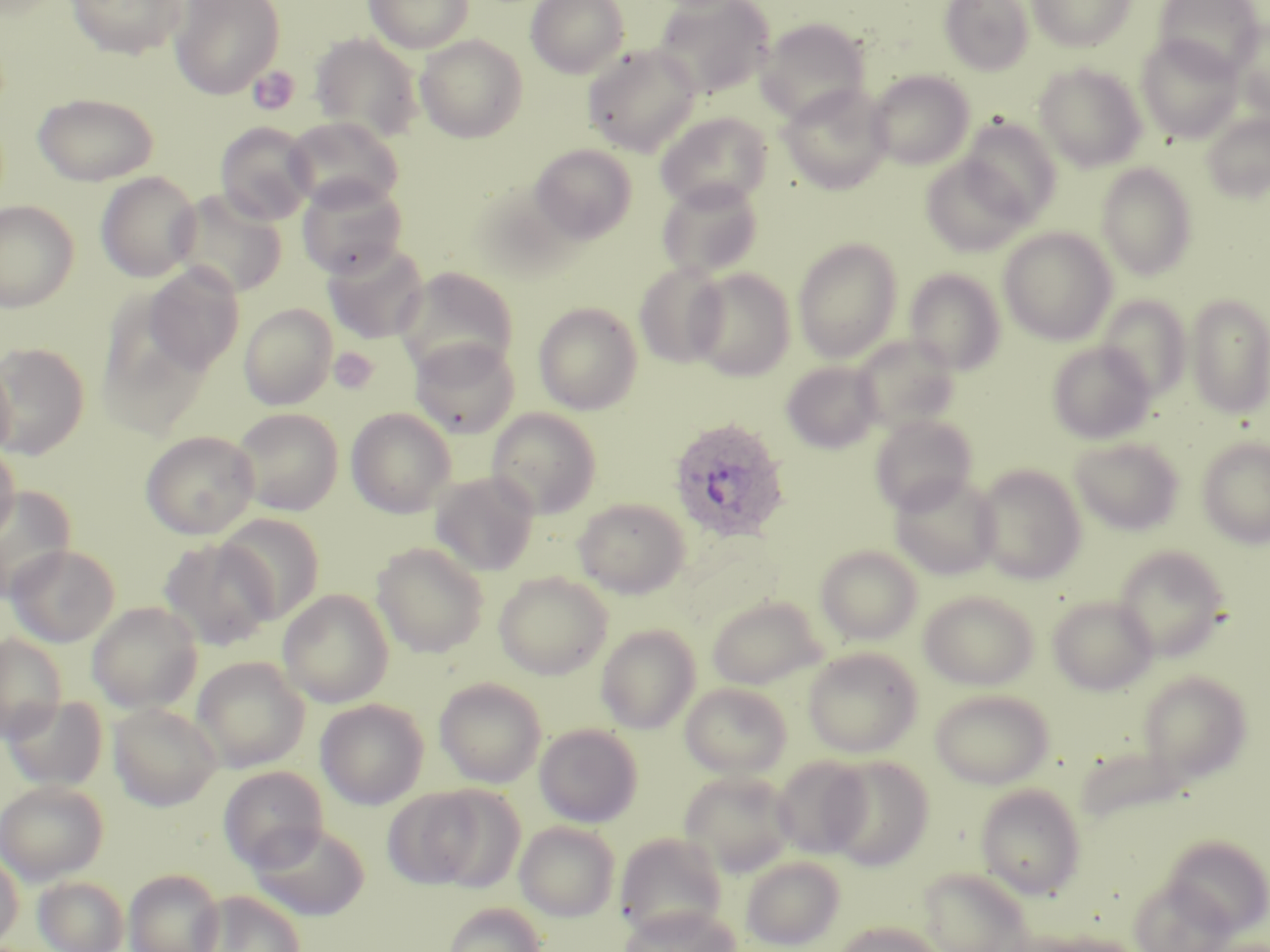

Approximate bounding boxes as (x1,y1)-(x2,y2) corner pairs in pixels. Platelet locations: (247,65)-(300,116), (329,347)-(380,394). Uninfected red blood cell locations: (67,0)-(188,59), (170,0)-(285,98), (363,0)-(474,52), (526,0)-(629,78), (654,0)-(775,99), (940,0)-(1034,75), (1027,0)-(1136,51), (1154,0)-(1263,77), (756,17)-(871,124), (1229,18)-(1270,119), (310,32)-(424,142), (415,35)-(528,142), (1136,35)-(1243,142), (582,43)-(702,156), (1034,63)-(1146,171), (867,70)-(975,170), (778,84)-(892,194), (32,92)-(159,186), (656,112)-(772,211), (1201,112)-(1270,203), (285,116)-(404,212), (959,117)-(1062,225), (215,122)-(317,225), (530,143)-(637,244), (920,155)-(1031,256), (1095,162)-(1199,280), (95,171)-(202,282), (297,176)-(408,279), (656,179)-(765,280), (169,189)-(287,299), (0,199)-(80,312), (998,227)-(1117,345), (793,237)-(902,362), (322,241)-(430,344), (634,262)-(730,368), (144,264)-(244,374), (394,267)-(519,377), (688,267)-(796,381), (904,268)-(1006,375), (1185,293)-(1270,418), (1096,295)-(1191,402), (96,296)-(216,436), (533,302)-(643,415), (239,303)-(337,410), (852,335)-(960,433), (409,338)-(521,438), (1047,341)-(1155,444), (0,342)-(90,459), (0,354)-(15,463), (781,361)-(882,453), (232,408)-(343,516), (346,408)-(456,518), (486,408)-(602,518), (869,414)-(978,515), (141,430)-(259,539), (1069,437)-(1184,536), (1197,437)-(1270,547), (0,441)-(20,546), (973,464)-(1087,584), (430,471)-(540,576), (888,473)-(1001,580), (1,485)-(76,603), (573,497)-(691,598), (217,513)-(325,624), (158,537)-(277,652), (372,542)-(489,658), (6,544)-(119,647), (816,545)-(923,645), (1112,545)-(1231,661), (493,572)-(613,679), (278,589)-(394,707), (919,590)-(1039,690), (706,595)-(826,690), (1047,595)-(1158,695), (87,601)-(203,713), (596,624)-(700,734), (0,635)-(67,741), (802,647)-(923,758), (192,656)-(309,772), (1138,670)-(1253,783), (434,677)-(546,788), (680,682)-(792,779), (929,689)-(1055,788), (3,695)-(108,792), (316,698)-(429,810), (108,702)-(222,810), (534,724)-(642,827), (1075,744)-(1188,827), (771,755)-(872,860), (823,755)-(935,870), (219,766)-(329,871), (679,770)-(797,876), (0,780)-(108,884), (975,783)-(1086,899), (383,785)-(500,890), (247,821)-(371,921), (514,822)-(620,921), (614,832)-(728,940), (1162,834)-(1270,935), (0,849)-(24,948), (740,855)-(845,950), (123,868)-(225,952), (918,868)-(1035,951), (33,875)-(130,952), (1128,877)-(1235,952), (192,890)-(306,952), (441,902)-(547,952), (618,903)-(742,952), (832,920)-(948,952), (1031,932)-(1148,952). Plasmodium ovale-infected red blood cell locations: (668,417)-(792,543). Slide-level diagnosis: Plasmodium ovale. Thin blood smear. Optical microscopy. Image is 1270×952 pixels. One field of a larger specimen. 1000x magnification. May-Grünwald-Giemsa-stained preparation.